Comment on the morphology of the red blood cells.
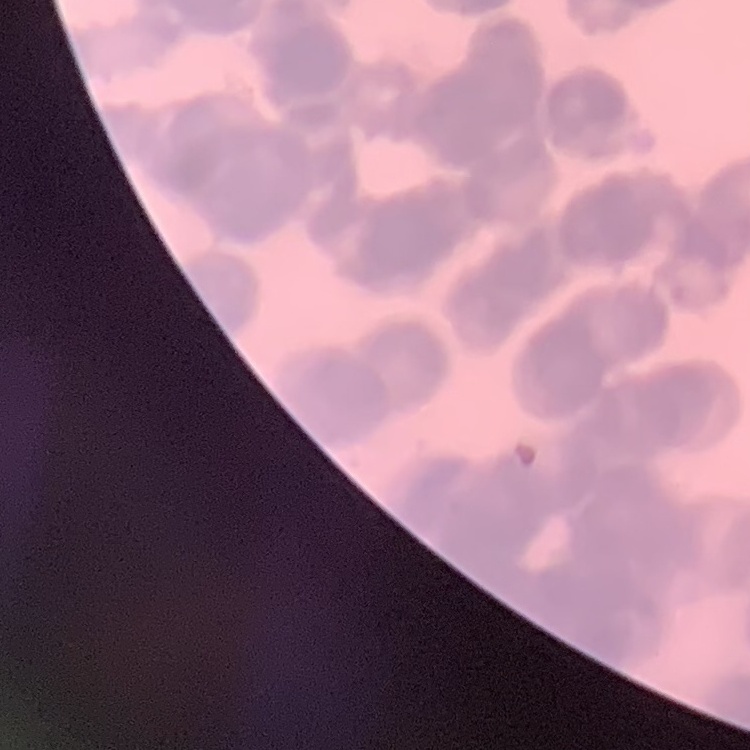

They show rouleaux formation.

{
  "stain": "Field's or Giemsa",
  "preparation": "thin blood film",
  "image_type": "one tile cut from a larger photomicrograph"
}